Classify this cell by malaria status.
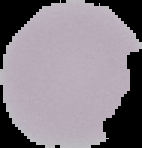
It is uninfected.

Cell region segmented out of the field of view; the surrounding area is masked to black. From a thin blood smear. Image is 142×148 pixels.